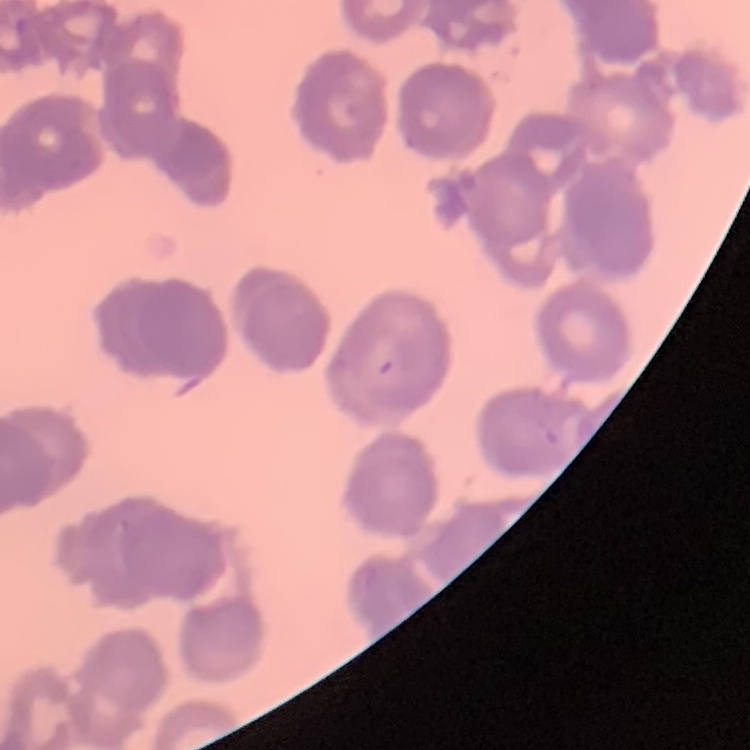
erythrocyte morphology = rouleaux formation
image type = one tile cut from a larger photomicrograph
preparation = thin blood smear
stain = Field's or Giemsa